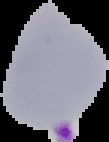

Cell region segmented out of the field of view; the surrounding area is masked to black. Image is 109×142 pixels. Result: malaria parasites identified. From a thin blood film.